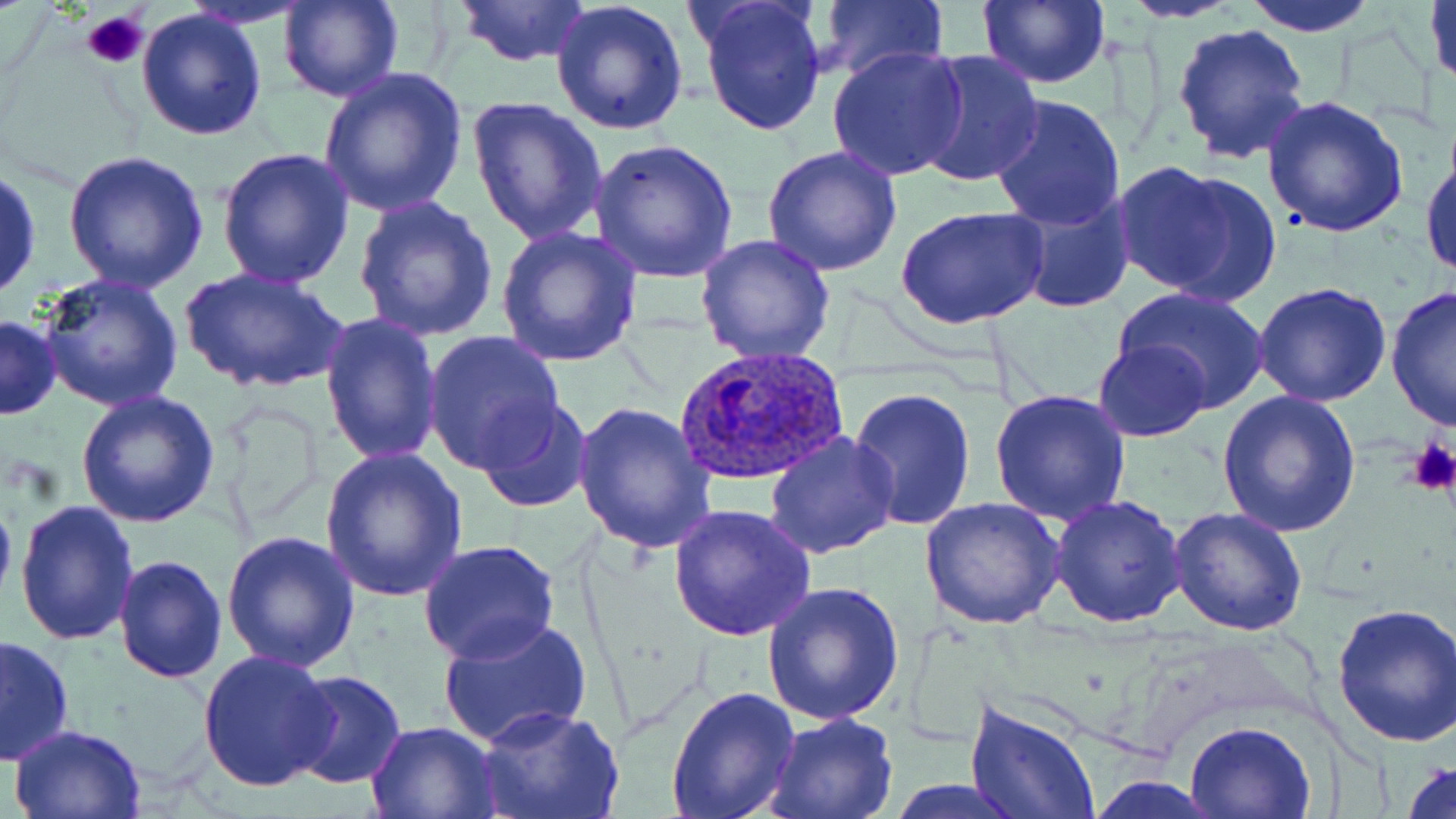

slide_level_diagnosis: Plasmodium ovale
image_size: 1456×819 pixels
platelet_locations: 'approximate bounding boxes as [x1, y1, x2, y2] in pixels: [81, 10, 150, 70], [1407, 438, 1456, 495]'
modality: optical microscopy
uninfected_red_blood_cell_locations: 'approximate bounding boxes as [x1, y1, x2, y2] in pixels: [278, 0, 403, 103], [454, 0, 591, 68], [695, 0, 828, 138], [976, 0, 1110, 89], [1240, 0, 1383, 36], [1426, 0, 1456, 94], [550, 1, 691, 137], [817, 1, 948, 82], [1120, 1, 1244, 22], [137, 6, 269, 141], [1171, 22, 1312, 166], [826, 43, 970, 181], [912, 50, 1045, 190], [316, 67, 467, 217], [988, 93, 1130, 230], [1259, 93, 1409, 238], [466, 95, 608, 246], [588, 138, 740, 282], [1421, 145, 1455, 282], [215, 147, 355, 290], [762, 147, 903, 279], [60, 149, 209, 294], [1111, 162, 1272, 303], [0, 164, 42, 303], [1008, 187, 1138, 314], [353, 197, 499, 343], [897, 205, 1049, 332], [494, 224, 643, 367], [694, 233, 836, 365], [178, 266, 348, 396], [35, 272, 186, 413], [1252, 283, 1391, 407], [1113, 286, 1270, 412], [1384, 287, 1455, 432], [319, 311, 444, 467], [1, 314, 62, 419], [423, 329, 567, 474], [1093, 339, 1211, 441], [847, 385, 979, 532], [988, 387, 1134, 526], [76, 389, 222, 527], [1217, 390, 1361, 537], [476, 399, 593, 515], [570, 401, 717, 553], [764, 432, 900, 559], [320, 448, 469, 602], [0, 479, 17, 618], [1049, 495, 1187, 628], [920, 496, 1065, 630], [14, 499, 139, 647], [667, 503, 817, 641], [1167, 507, 1308, 636], [221, 529, 361, 671], [419, 540, 560, 665], [113, 554, 228, 684], [763, 582, 902, 725], [1331, 599, 1456, 747], [437, 615, 592, 749], [0, 633, 75, 766], [198, 652, 339, 794], [286, 670, 406, 789], [666, 684, 800, 819], [966, 697, 1101, 819], [479, 708, 623, 819], [762, 712, 898, 819], [1185, 719, 1316, 818], [365, 720, 500, 817], [10, 723, 149, 817], [1400, 755, 1456, 819], [1087, 777, 1224, 817], [885, 780, 1029, 816]'
field_of_view: single
plasmodium_ovale_infected_red_blood_cell_locations: 'approximate bounding boxes as [x1, y1, x2, y2] in pixels: [676, 347, 850, 488]'
stain: May-Grünwald-Giemsa
preparation: thin blood smear
magnification: 1000x